Assess this cell for malaria.
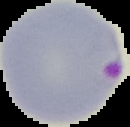

Parasitized.

From a thin blood film. Cell region segmented out of the field of view; the surrounding area is masked to black. Image is 130×127 pixels.